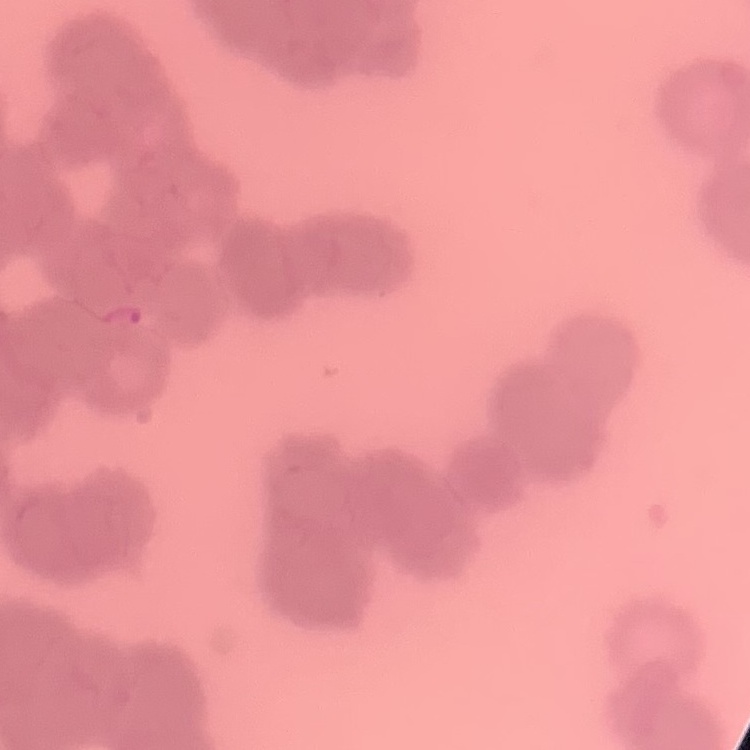 The red blood cells exhibit rouleaux formation. Stained with either Field's or Giemsa. Thin blood smear. One tile cut from a larger photomicrograph.